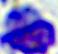
A white blood cell is shown. Photomicrograph. Captured at 400x magnification.